Classify this cell by malaria status.
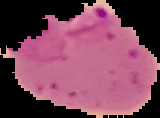

Parasitized.

image type = cell region segmented out of the field of view; surrounding area masked to black
image size = 160×118 pixels
preparation = thin blood film